Point out each Plasmodium parasite.
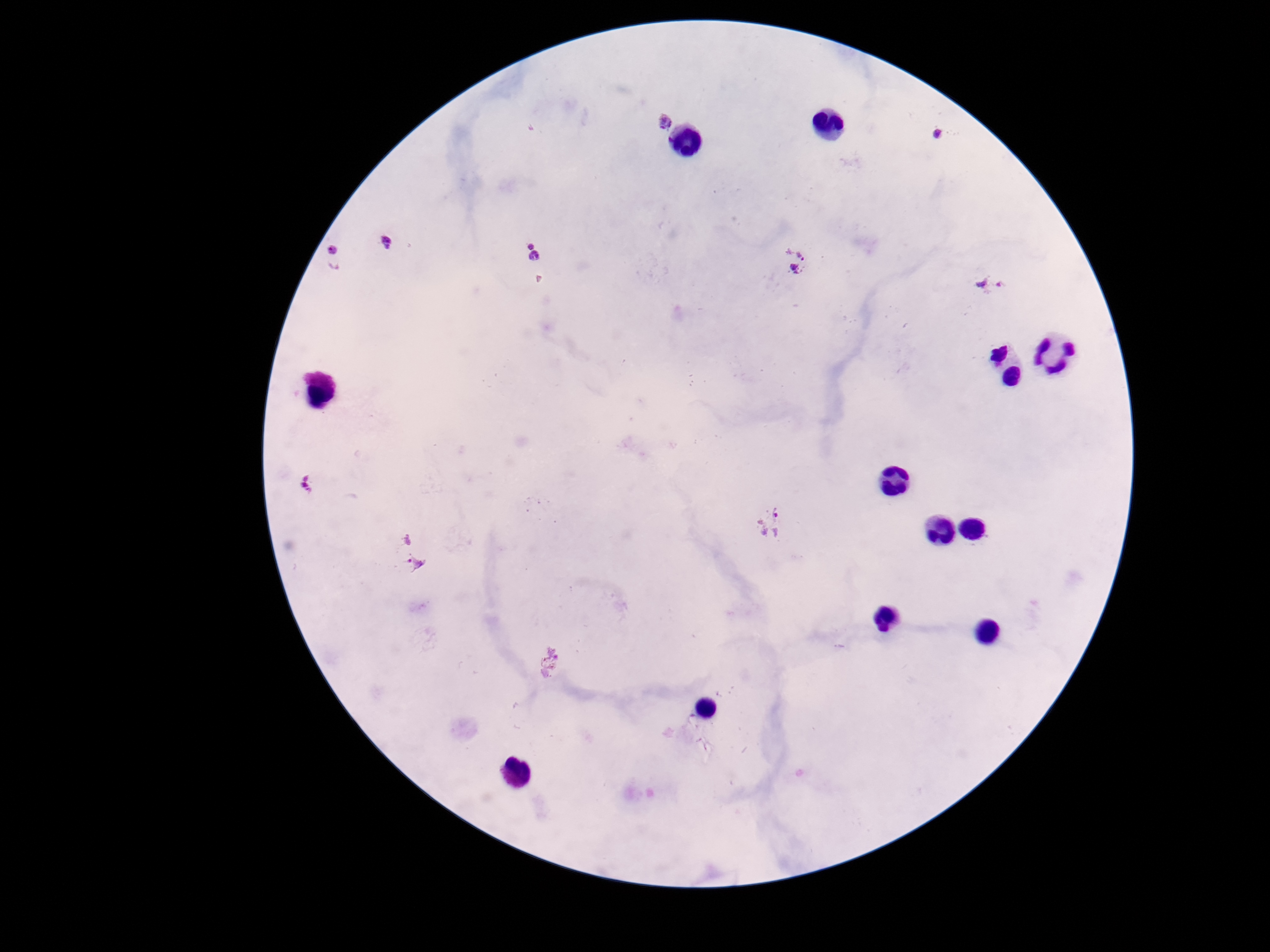

Approximate centers as {x, y} in pixels.
Plasmodium parasites: {661, 117}, {941, 134}, {390, 242}, {334, 252}, {535, 253}, {796, 262}, {991, 286}, {306, 483}, {773, 523}, {410, 551}.

One field from this slide. 100x magnification. Patient malaria status: positive. Image is 1270×952 pixels. Giemsa stain. Smartphone photograph taken through the microscope eyepiece. Thick blood film.